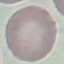

malaria status = uninfected
capture = smartphone camera at the microscope eyepiece
preparation = thin blood smear
image type = automatically extracted cell patch, resized to 64 × 64 pixels
stain = Giemsa